Locate every Plasmodium parasite.
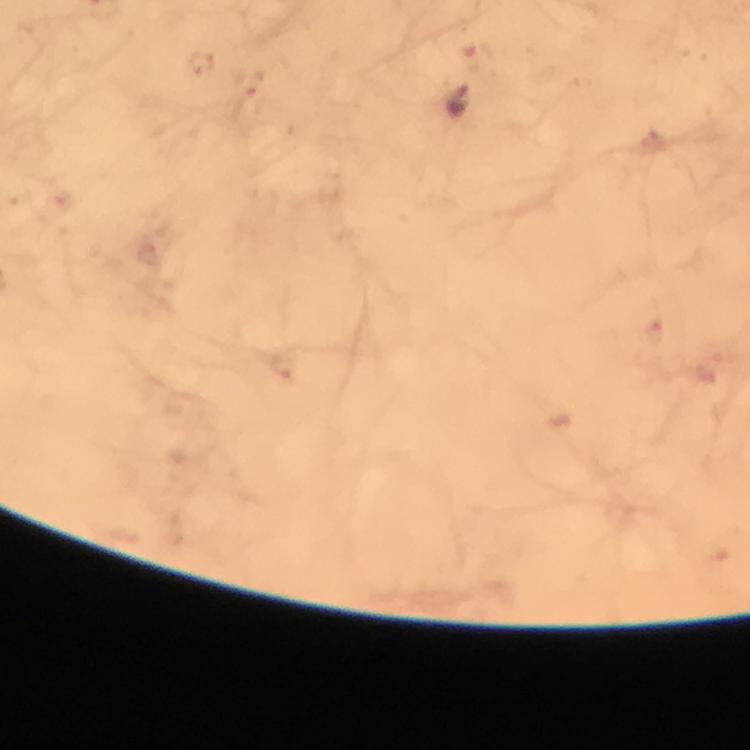
Approximate centers as [x, y] in pixels.
Plasmodium parasites: [201, 65], [248, 87], [458, 104], [659, 327].

Summary:
  - Image size: 750×750 pixels
  - Magnification: 100x
  - Context: from a diagnostic examination for malaria
  - Cropped from: one field of view
  - Preparation: thick blood smear
  - Capture: smartphone photograph through a microscope
  - Stain: Giemsa
  - Immersion oil: used